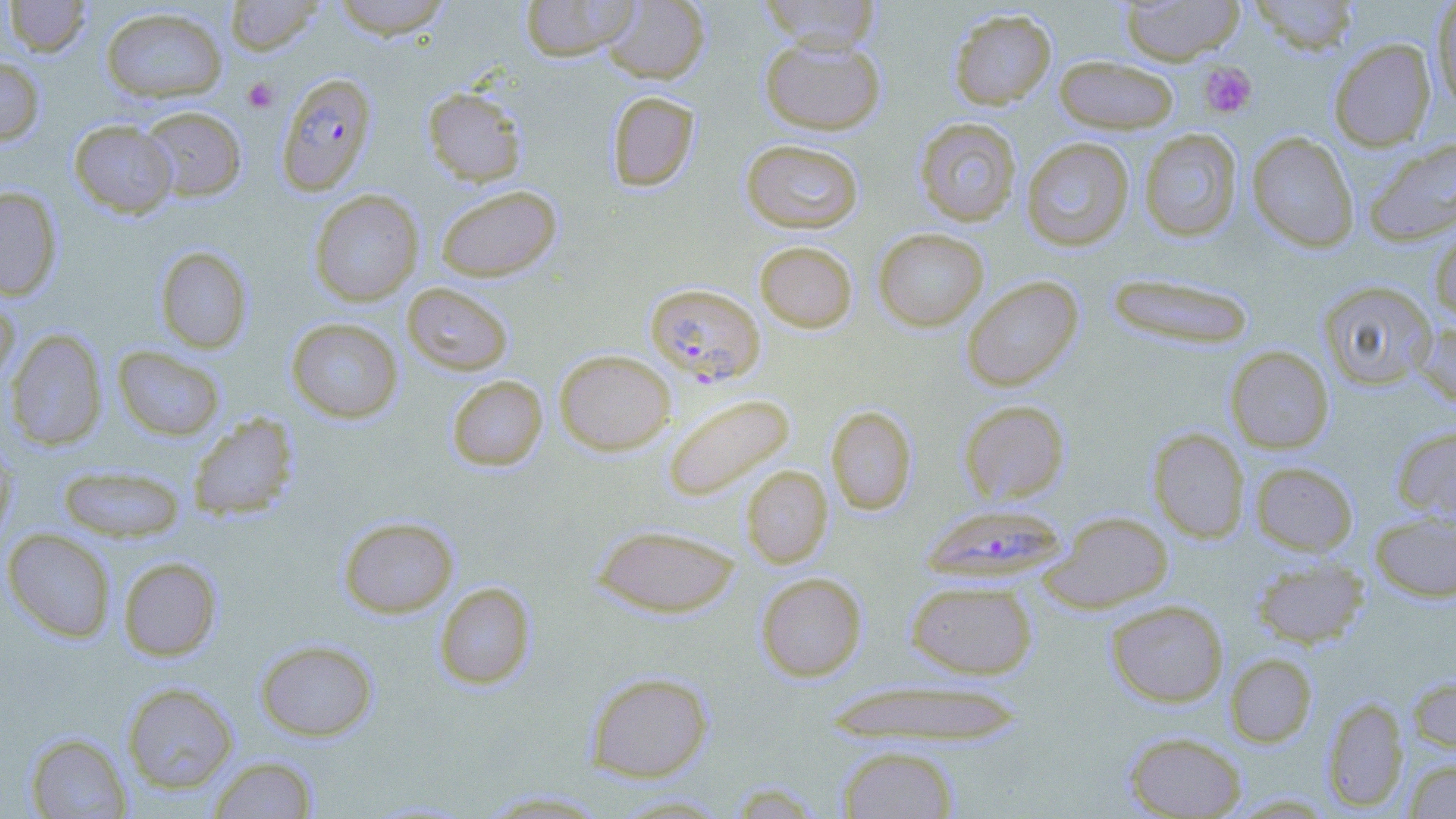

Approximate bounding boxes as named x1/y1/x2/y2 corners in pixels. Plasmodium falciparum-infected red blood cell locations (subset): (x1=276, y1=72, x2=378, y2=196), (x1=920, y1=503, x2=1069, y2=586). Uninfected red blood cell locations (subset): (x1=5, y1=0, x2=92, y2=58), (x1=224, y1=0, x2=325, y2=56), (x1=330, y1=0, x2=453, y2=39), (x1=520, y1=0, x2=640, y2=61), (x1=603, y1=0, x2=709, y2=84), (x1=758, y1=0, x2=882, y2=54), (x1=1119, y1=0, x2=1244, y2=64), (x1=1247, y1=0, x2=1361, y2=55), (x1=1431, y1=0, x2=1456, y2=108), (x1=100, y1=6, x2=227, y2=103), (x1=948, y1=8, x2=1056, y2=110), (x1=760, y1=34, x2=886, y2=135), (x1=1328, y1=37, x2=1437, y2=151), (x1=1054, y1=56, x2=1180, y2=134), (x1=0, y1=57, x2=45, y2=145), (x1=423, y1=86, x2=527, y2=186), (x1=606, y1=90, x2=699, y2=192), (x1=137, y1=105, x2=246, y2=202), (x1=914, y1=117, x2=1022, y2=226), (x1=69, y1=119, x2=178, y2=218), (x1=1139, y1=128, x2=1243, y2=241), (x1=1247, y1=131, x2=1359, y2=252), (x1=1362, y1=136, x2=1456, y2=247), (x1=1021, y1=137, x2=1135, y2=251), (x1=741, y1=139, x2=864, y2=234), (x1=435, y1=185, x2=562, y2=282), (x1=0, y1=186, x2=63, y2=301), (x1=309, y1=190, x2=424, y2=307), (x1=1429, y1=221, x2=1456, y2=324), (x1=873, y1=227, x2=988, y2=331), (x1=754, y1=240, x2=858, y2=333), (x1=154, y1=246, x2=253, y2=354), (x1=1106, y1=272, x2=1256, y2=349), (x1=961, y1=275, x2=1084, y2=391), (x1=1318, y1=280, x2=1438, y2=391), (x1=402, y1=282, x2=514, y2=376), (x1=0, y1=292, x2=20, y2=392), (x1=285, y1=317, x2=404, y2=423), (x1=1413, y1=320, x2=1456, y2=409), (x1=5, y1=329, x2=107, y2=451), (x1=112, y1=345, x2=225, y2=441), (x1=1225, y1=346, x2=1334, y2=454), (x1=554, y1=349, x2=676, y2=455), (x1=446, y1=375, x2=548, y2=471), (x1=664, y1=394, x2=795, y2=500), (x1=959, y1=400, x2=1070, y2=505), (x1=826, y1=405, x2=917, y2=515), (x1=187, y1=412, x2=299, y2=521), (x1=1392, y1=425, x2=1456, y2=526), (x1=1148, y1=427, x2=1250, y2=543), (x1=0, y1=440, x2=17, y2=549), (x1=1250, y1=461, x2=1358, y2=556), (x1=57, y1=464, x2=186, y2=543), (x1=741, y1=465, x2=833, y2=568), (x1=1044, y1=511, x2=1174, y2=612), (x1=1370, y1=511, x2=1456, y2=602), (x1=338, y1=515, x2=458, y2=618), (x1=592, y1=523, x2=741, y2=618), (x1=2, y1=528, x2=116, y2=643), (x1=1250, y1=556, x2=1369, y2=648), (x1=118, y1=557, x2=222, y2=661), (x1=755, y1=572, x2=867, y2=682), (x1=905, y1=579, x2=1037, y2=679), (x1=434, y1=582, x2=536, y2=690), (x1=1106, y1=599, x2=1229, y2=707), (x1=255, y1=639, x2=378, y2=741), (x1=1225, y1=652, x2=1317, y2=748), (x1=585, y1=670, x2=714, y2=782), (x1=1407, y1=674, x2=1456, y2=755), (x1=825, y1=679, x2=1026, y2=746), (x1=121, y1=682, x2=239, y2=794), (x1=1322, y1=696, x2=1408, y2=812), (x1=24, y1=731, x2=131, y2=818), (x1=1124, y1=731, x2=1247, y2=818), (x1=836, y1=745, x2=959, y2=819), (x1=207, y1=755, x2=318, y2=818), (x1=1404, y1=757, x2=1456, y2=818), (x1=728, y1=782, x2=825, y2=818), (x1=478, y1=790, x2=615, y2=817), (x1=608, y1=794, x2=735, y2=817). Platelet locations: (x1=1199, y1=61, x2=1257, y2=118), (x1=243, y1=78, x2=279, y2=112). Slide-level diagnosis: Plasmodium falciparum. Single field of view. Image is 1456×819 pixels. 1000x magnification. Light microscopy. May-Grünwald-Giemsa stain. Thin blood smear.